Classify this cell by malaria status.
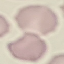

Uninfected.

Automatically extracted cell patch, resized to 64 × 64 pixels. Giemsa-stained preparation. Thin smear of blood. Acquired by smartphone through the microscope eyepiece.